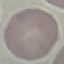 Result: no malaria parasites seen. Giemsa stain. Automatically extracted cell patch, resized to 64 × 64 pixels. Acquired by smartphone through the microscope eyepiece. Thin blood film.